Identify the blood parasite species.
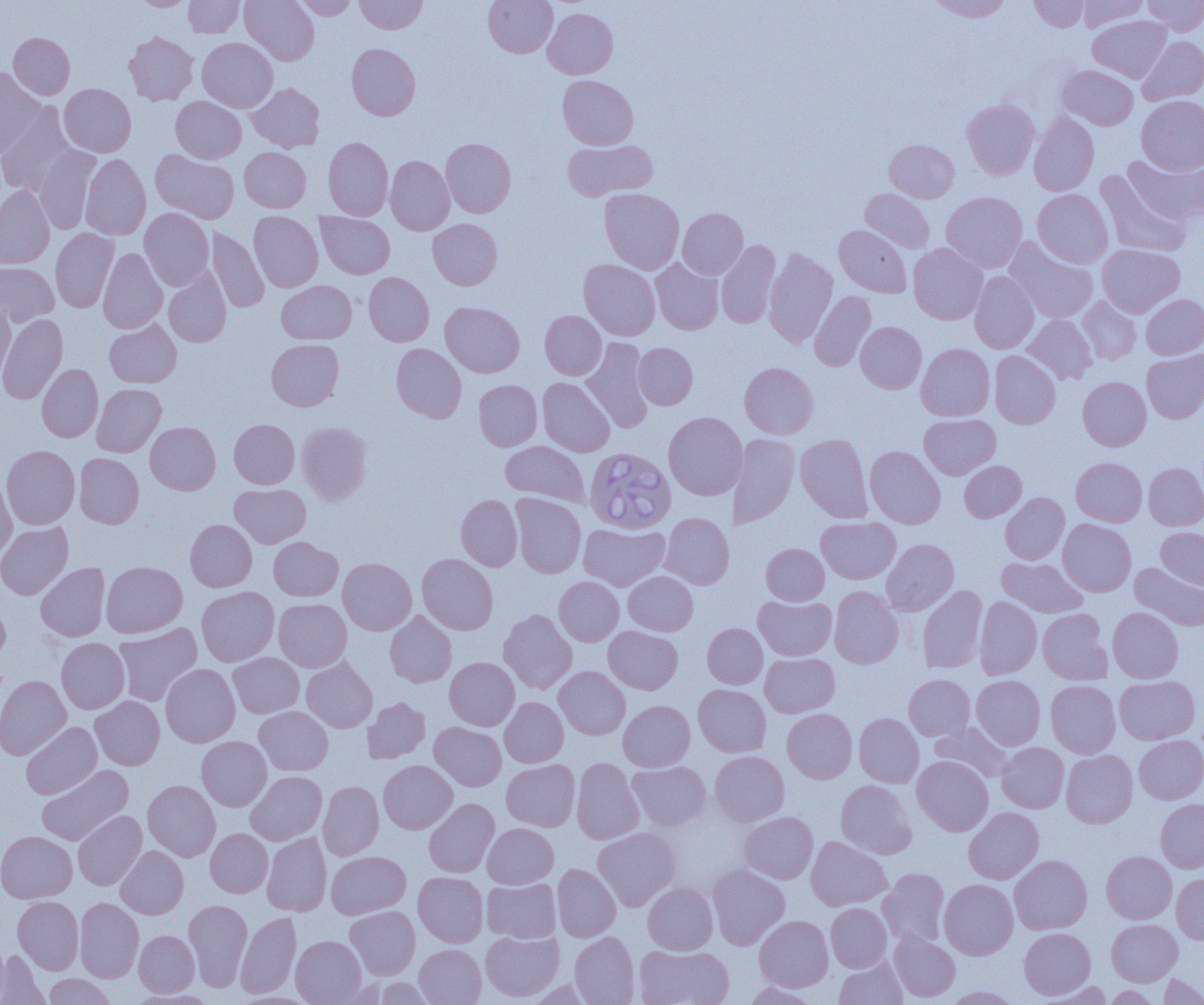

Babesia divergens.

Approximate bounding boxes as (x1,y1)-(x2,y2) corner pairs in pixels. Uninfected red blood cell locations: (131,0)-(193,10), (184,0)-(244,38), (240,0)-(319,65), (294,0)-(358,20), (355,0)-(427,34), (484,0)-(558,57), (927,0)-(1014,21), (1029,0)-(1090,32), (1077,0)-(1148,31), (1143,0)-(1204,35), (543,8)-(618,78), (1087,15)-(1171,82), (124,31)-(198,105), (9,33)-(75,99), (1137,36)-(1204,105), (197,37)-(278,112), (347,43)-(421,120), (1057,65)-(1138,130), (0,67)-(46,157), (558,75)-(638,149), (246,83)-(324,152), (59,84)-(136,157), (1136,96)-(1204,174), (171,97)-(246,163), (962,99)-(1039,180), (0,103)-(76,196), (1029,112)-(1099,195), (323,137)-(393,220), (441,138)-(516,218), (884,139)-(959,202), (562,140)-(658,201), (33,144)-(100,232), (239,147)-(311,212), (150,149)-(239,223), (1125,152)-(1204,224), (80,153)-(151,240), (385,156)-(455,235), (1095,169)-(1190,258), (0,186)-(55,268), (599,188)-(684,274), (859,188)-(934,253), (1032,189)-(1113,268), (942,191)-(1028,273), (140,208)-(214,290), (677,208)-(748,279), (249,211)-(323,292), (316,212)-(394,279), (428,218)-(502,290), (834,225)-(912,297), (50,228)-(118,312), (206,228)-(269,312), (1004,237)-(1098,323), (716,240)-(781,329), (908,243)-(987,324), (1098,243)-(1185,317), (98,248)-(167,333), (764,248)-(837,348), (650,258)-(724,334), (578,259)-(660,340), (0,262)-(58,327), (164,269)-(231,347), (969,271)-(1040,353), (364,272)-(434,346), (277,280)-(356,343), (809,291)-(876,371), (1141,294)-(1204,359), (1078,296)-(1141,364), (0,300)-(15,381), (440,302)-(525,377), (540,310)-(606,379), (0,314)-(68,404), (1022,314)-(1098,385), (105,319)-(181,388), (856,321)-(926,393), (581,338)-(654,432), (267,339)-(344,411), (633,342)-(697,409), (391,343)-(467,423), (916,343)-(995,421), (1142,349)-(1204,423), (989,350)-(1061,429), (739,362)-(818,438), (37,364)-(103,442), (1078,377)-(1151,450), (537,378)-(615,457), (474,380)-(542,451), (92,384)-(166,457), (663,411)-(748,500), (918,414)-(1000,479), (229,419)-(299,488), (296,421)-(373,505), (145,422)-(220,494), (729,433)-(800,529), (795,434)-(872,522), (500,440)-(589,506), (1,445)-(80,529), (865,446)-(945,529), (74,453)-(144,528), (1071,457)-(1147,526), (960,461)-(1026,522), (1143,463)-(1204,530), (1,477)-(16,561), (230,484)-(310,548), (511,493)-(586,578), (1000,493)-(1070,564), (456,494)-(522,570), (660,512)-(734,589), (816,517)-(900,584), (186,519)-(257,591), (1057,519)-(1136,596), (0,522)-(73,599), (579,523)-(669,591), (1156,527)-(1204,590), (269,537)-(343,600), (882,539)-(959,615), (761,543)-(829,605), (417,554)-(498,634), (997,557)-(1087,617), (338,558)-(417,635), (101,561)-(187,637), (1129,562)-(1204,631), (36,563)-(110,641), (623,571)-(698,635), (554,576)-(624,645), (917,585)-(987,673), (197,586)-(279,666), (829,586)-(904,668), (753,595)-(836,660), (975,597)-(1042,679), (274,598)-(352,671), (0,600)-(10,666), (1108,607)-(1183,683), (498,609)-(577,694), (1038,609)-(1112,685), (385,611)-(456,687), (113,623)-(202,706), (702,623)-(767,688), (603,626)-(683,694), (56,638)-(129,714), (228,652)-(304,718), (760,653)-(839,717), (302,657)-(377,732), (445,657)-(519,730), (161,663)-(240,747), (554,666)-(630,739), (0,675)-(71,760), (904,675)-(975,740), (971,675)-(1045,750), (1114,676)-(1200,744), (1046,680)-(1120,758), (693,684)-(771,757), (90,696)-(164,770), (363,697)-(431,763), (500,697)-(568,767), (618,700)-(695,771), (254,706)-(333,775), (782,708)-(857,783), (854,713)-(924,787), (21,722)-(102,799), (429,722)-(506,791), (930,722)-(1013,782), (1134,735)-(1204,804), (196,736)-(271,811), (997,742)-(1069,813), (1061,750)-(1138,828), (709,751)-(789,826), (912,756)-(993,835), (571,758)-(644,845), (501,759)-(580,831), (378,760)-(457,834), (627,761)-(711,832), (37,765)-(133,845), (246,771)-(327,845), (143,780)-(220,861), (836,780)-(917,858), (318,781)-(384,860), (423,798)-(499,878), (1156,799)-(1204,873), (964,807)-(1044,884), (73,810)-(147,890), (738,811)-(818,884), (483,823)-(558,888), (593,827)-(681,911), (205,828)-(273,897), (0,831)-(77,903), (262,832)-(332,916), (806,836)-(891,910), (116,846)-(188,919), (326,851)-(410,919), (1101,851)-(1177,924), (1009,855)-(1092,934), (552,863)-(621,942), (707,864)-(790,950), (877,868)-(949,948), (413,872)-(488,947), (1172,873)-(1204,943), (482,878)-(560,943), (939,879)-(1018,959), (643,882)-(718,954), (13,896)-(84,974), (74,898)-(144,982), (183,899)-(253,990), (826,903)-(892,972), (345,906)-(420,979), (236,912)-(301,998), (754,915)-(833,992), (1107,919)-(1183,986), (1019,927)-(1095,999), (480,929)-(563,1002), (134,930)-(199,997), (889,931)-(960,1002), (570,932)-(639,1004), (291,935)-(366,1004), (415,944)-(486,1004), (635,944)-(733,1005), (0,950)-(48,1005), (834,956)-(908,1004), (1158,973)-(1204,1005), (43,974)-(115,1005), (371,977)-(435,1005), (528,979)-(601,1005), (1037,981)-(1115,1004), (742,982)-(822,1004), (1104,985)-(1160,1004), (942,986)-(1021,1004), (126,989)-(219,1004). Babesia divergens-infected red blood cell locations: (583,447)-(676,534). Captured at 1000x magnification. Optical microscopy. Image is 1204×1005 pixels. Single field of view. Thin blood film.